Locate every Plasmodium ovale-infected red blood cell.
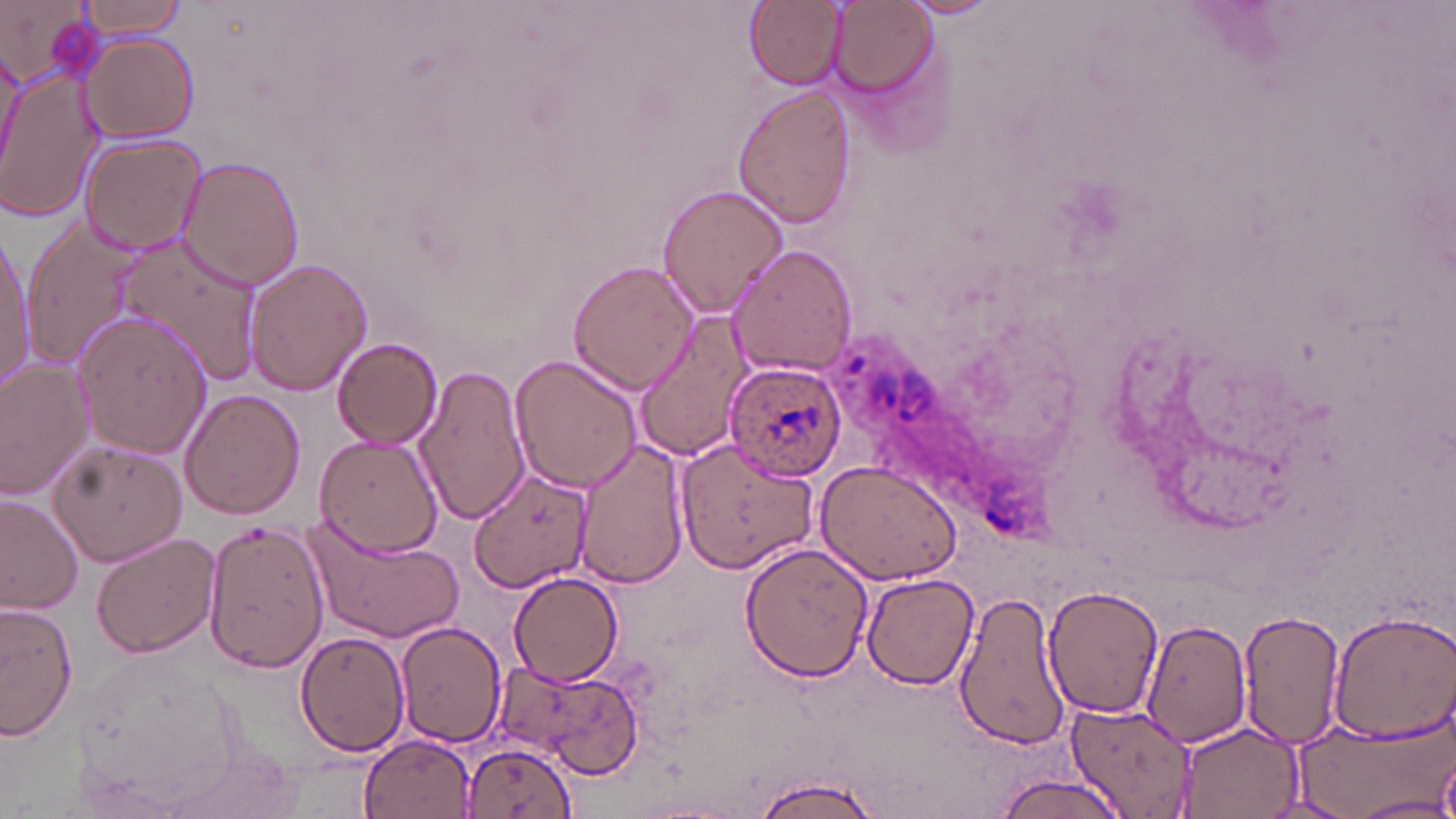

Approximate bounding boxes as (x1,y1)-(x2,y2) corner pairs in pixels.
Plasmodium ovale-infected red blood cells: (724,361)-(848,480).

Uninfected red blood cell locations: (72,0)-(192,39), (745,0)-(844,88), (900,0)-(1005,20), (1,2)-(100,89), (829,2)-(933,96), (81,34)-(199,143), (0,71)-(104,223), (733,85)-(857,230), (78,135)-(206,256), (178,157)-(305,290), (656,184)-(792,321), (24,218)-(143,366), (0,232)-(35,392), (113,235)-(262,387), (728,244)-(857,377), (246,258)-(371,397), (567,258)-(697,396), (74,311)-(211,458), (635,312)-(751,463), (333,338)-(443,449), (510,353)-(642,492), (0,359)-(95,496), (415,362)-(530,527), (180,389)-(305,519), (313,435)-(443,556), (674,438)-(818,571), (48,439)-(188,568), (575,441)-(691,590), (814,459)-(964,584), (470,466)-(594,594), (0,494)-(82,616), (300,513)-(467,642), (203,519)-(330,672), (91,533)-(220,659), (740,543)-(873,684), (509,571)-(625,687), (862,574)-(978,691), (1041,584)-(1164,721), (953,588)-(1071,753), (1,601)-(78,742), (1238,609)-(1346,747), (1326,610)-(1456,742), (1142,618)-(1250,746), (394,622)-(504,748), (294,631)-(410,757), (516,666)-(641,781), (1064,701)-(1193,816), (1285,719)-(1450,818), (1174,721)-(1303,819), (358,733)-(475,816), (459,740)-(576,816), (992,773)-(1129,818), (751,774)-(884,818), (1347,795)-(1456,818). Slide-level diagnosis: Plasmodium ovale. May-Grünwald-Giemsa-stained preparation. Single field of view. Image is 1456×819 pixels. Captured at 1000x magnification. Thin blood film. Light microscopy.